Locate every Plasmodium parasite and every leukocyte.
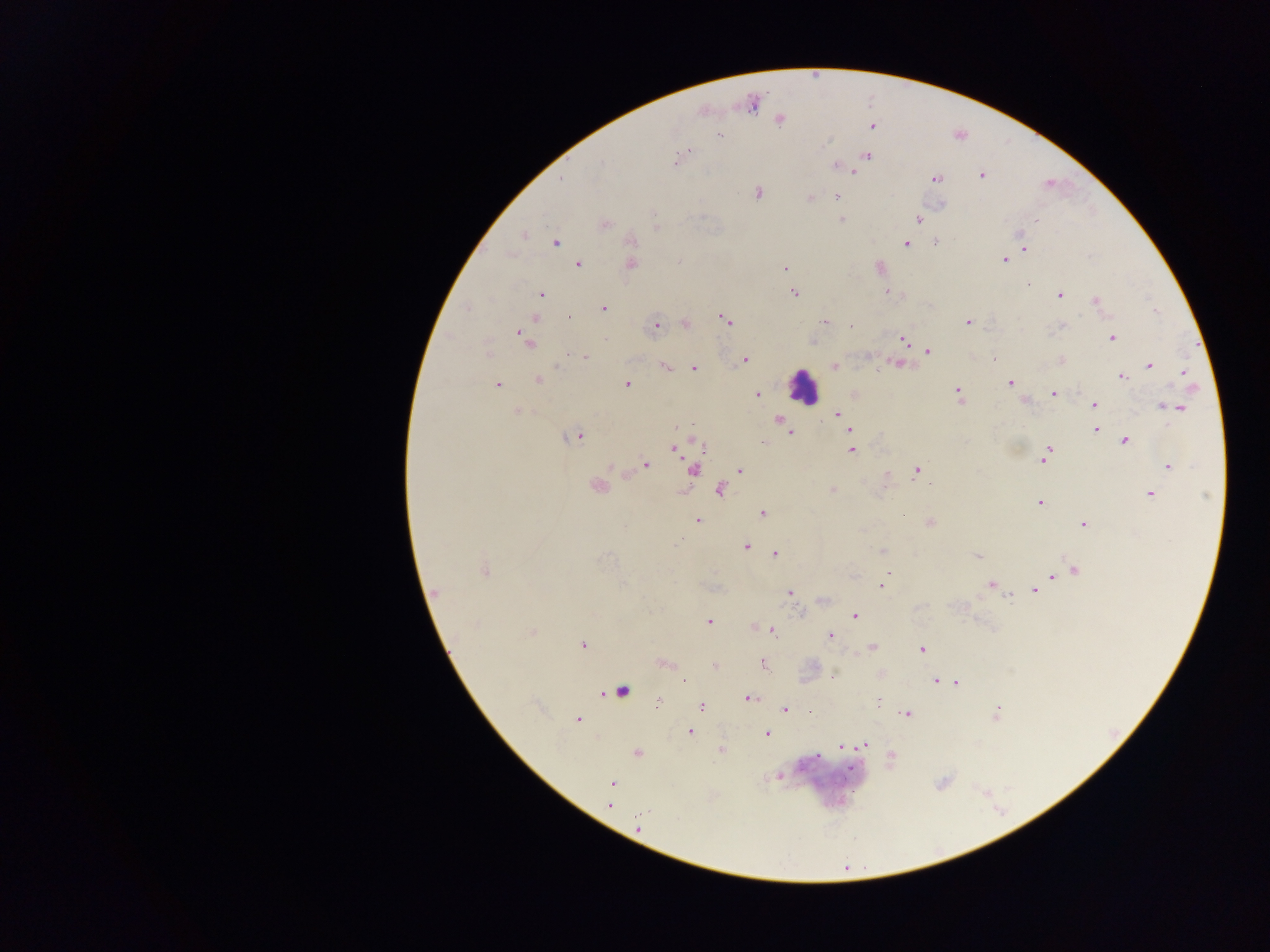
Approximate centers as {x, y} in pixels.
Plasmodium parasites: {753, 104}, {779, 119}, {870, 125}, {718, 135}, {866, 156}, {677, 160}, {837, 166}, {852, 169}, {980, 176}, {935, 179}, {758, 192}, {809, 197}, {836, 197}, {940, 205}, {842, 219}, {918, 219}, {1036, 219}, {603, 224}, {655, 226}, {524, 234}, {631, 240}, {556, 242}, {935, 242}, {906, 243}, {1024, 248}, {1003, 260}, {577, 264}, {630, 264}, {879, 267}, {785, 268}, {1028, 284}, {886, 291}, {794, 292}, {541, 294}, {1058, 295}, {1096, 300}, {603, 309}, {536, 317}, {724, 319}, {824, 321}, {967, 321}, {684, 323}, {655, 325}, {1061, 325}, {852, 328}, {520, 331}, {1112, 337}, {526, 339}, {812, 340}, {902, 340}, {926, 350}, {585, 357}, {995, 358}, {744, 359}, {1060, 360}, {897, 364}, {1148, 365}, {665, 366}, {834, 366}, {693, 368}, {1183, 372}, {1121, 376}, {538, 379}, {1010, 383}, {496, 384}, {627, 384}, {853, 393}, {1053, 393}, {757, 394}, {959, 395}, {1026, 400}, {1094, 405}, {1164, 406}, {1179, 407}, {516, 410}, {837, 414}, {778, 419}, {1096, 430}, {789, 433}, {574, 436}, {693, 440}, {1124, 440}, {685, 445}, {675, 447}, {850, 449}, {1045, 455}, {645, 464}, {1168, 466}, {693, 470}, {739, 470}, {916, 470}, {623, 473}, {883, 483}, {597, 486}, {719, 489}, {832, 490}, {1149, 494}, {1039, 502}, {901, 512}, {762, 513}, {697, 520}, {930, 522}, {1083, 524}, {746, 546}, {883, 551}, {775, 552}, {978, 556}, {1076, 569}, {484, 571}, {1052, 576}, {990, 584}, {881, 585}, {1039, 587}, {1033, 591}, {434, 593}, {789, 593}, {824, 599}, {854, 615}, {708, 622}, {754, 626}, {772, 630}, {531, 631}, {830, 635}, {582, 644}, {871, 647}, {922, 648}, {664, 663}, {762, 663}, {714, 665}, {880, 674}, {831, 675}, {684, 680}, {935, 680}, {956, 682}, {620, 690}, {747, 697}, {878, 701}, {656, 703}, {700, 705}, {784, 709}, {808, 711}, {907, 713}, {995, 713}, {577, 720}, {689, 732}, {765, 734}, {864, 744}, {840, 747}, {720, 750}, {637, 752}, {815, 756}, {891, 759}, {779, 775}, {612, 782}, {608, 804}, {637, 825}.
Leukocytes: {803, 387}.

preparation = thick blood smear
capture = mobile-phone photograph through a microscope
image size = 1270×952 pixels
field of view = single
country = Ghana